Comment on the morphology of the erythrocytes.
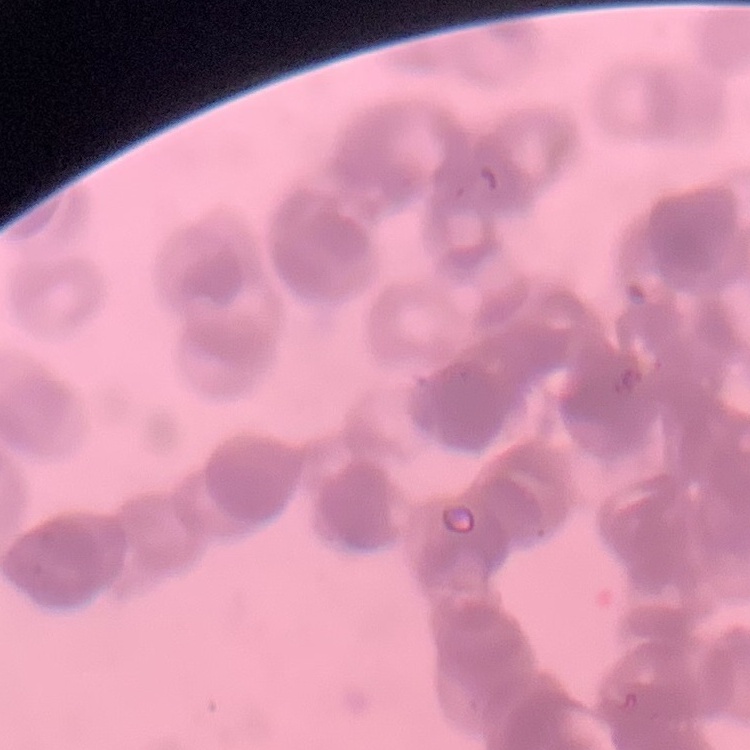
They show rouleaux formation.

Summary:
  - Preparation: thin blood film
  - Image type: square crop of a larger photomicrograph
  - Stain: Field's or Giemsa